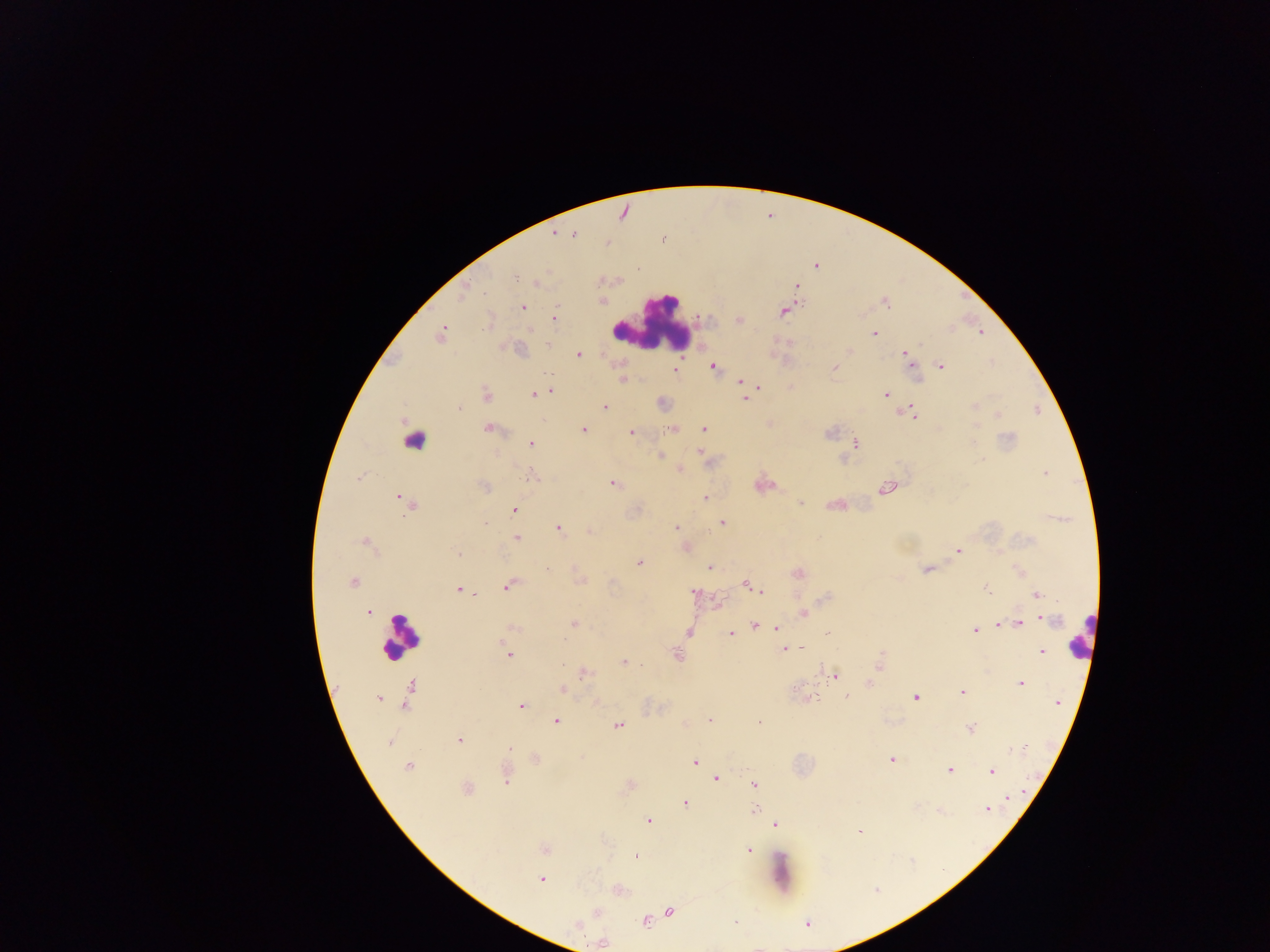 Approximate centers as {x, y} in pixels. Leukocyte locations: {652, 325}, {415, 440}, {400, 636}, {1080, 636}. Plasmodium parasite locations: {555, 234}, {574, 235}, {817, 267}, {516, 276}, {537, 282}, {797, 287}, {464, 293}, {885, 302}, {523, 307}, {783, 312}, {554, 318}, {739, 319}, {486, 322}, {441, 334}, {874, 334}, {519, 350}, {850, 350}, {578, 355}, {907, 356}, {910, 362}, {713, 366}, {940, 366}, {835, 367}, {675, 370}, {622, 380}, {740, 382}, {746, 384}, {758, 386}, {550, 390}, {542, 393}, {885, 394}, {486, 395}, {533, 395}, {745, 399}, {605, 406}, {974, 406}, {458, 408}, {912, 412}, {998, 415}, {488, 429}, {672, 429}, {704, 429}, {583, 430}, {631, 432}, {829, 433}, {1008, 438}, {531, 444}, {856, 444}, {699, 450}, {660, 456}, {680, 469}, {1045, 474}, {533, 475}, {359, 478}, {613, 483}, {484, 486}, {887, 488}, {400, 497}, {706, 498}, {408, 503}, {801, 503}, {515, 509}, {723, 523}, {485, 524}, {676, 527}, {559, 528}, {590, 531}, {516, 538}, {366, 541}, {958, 551}, {457, 554}, {639, 562}, {709, 568}, {926, 569}, {798, 573}, {353, 582}, {746, 584}, {508, 586}, {459, 589}, {754, 589}, {987, 589}, {761, 591}, {695, 593}, {1036, 595}, {824, 598}, {368, 613}, {803, 613}, {1048, 620}, {574, 623}, {1020, 623}, {1000, 625}, {755, 626}, {512, 627}, {761, 627}, {776, 627}, {976, 630}, {688, 633}, {827, 633}, {730, 634}, {801, 648}, {782, 650}, {505, 651}, {1041, 651}, {882, 654}, {508, 656}, {676, 656}, {623, 662}, {879, 665}, {823, 670}, {585, 673}, {836, 676}, {869, 683}, {1021, 683}, {410, 687}, {795, 688}, {563, 689}, {962, 691}, {847, 696}, {378, 698}, {813, 698}, {916, 698}, {405, 703}, {521, 706}, {556, 721}, {709, 721}, {760, 722}, {617, 725}, {971, 729}, {459, 740}, {510, 747}, {1016, 750}, {536, 759}, {891, 760}, {695, 762}, {408, 766}, {950, 770}, {992, 771}, {506, 775}, {717, 779}, {754, 785}, {467, 789}, {1010, 799}, {685, 803}, {987, 809}, {755, 810}, {939, 811}, {648, 821}, {776, 825}, {859, 833}, {544, 850}, {748, 850}, {637, 856}, {541, 880}, {670, 912}, {597, 913}, {645, 921}, {736, 923}, {807, 923}, {602, 943}. Photographed through a microscope with a mobile-phone camera. Collected in Ghana. Thick blood smear. Image is 1270×952 pixels. One field of view.